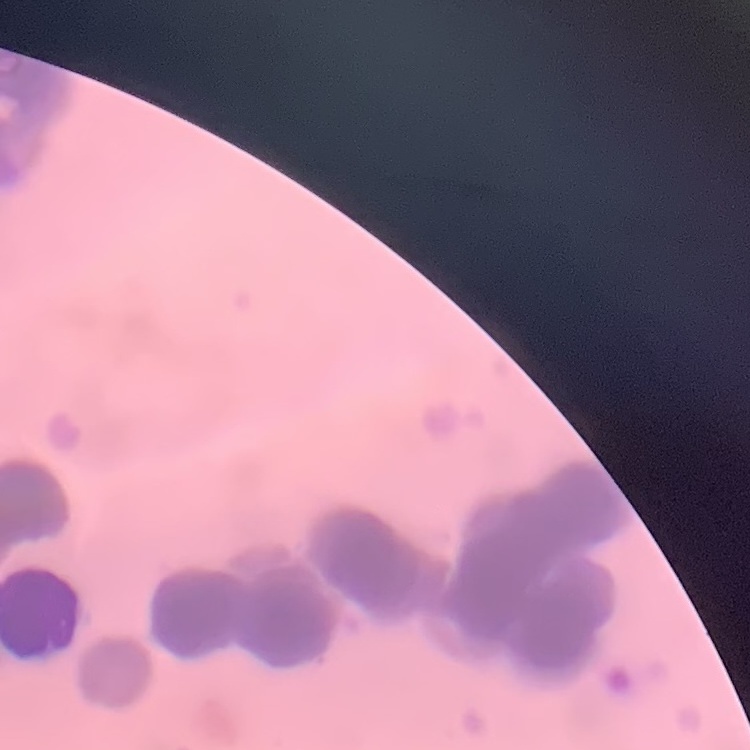

Summary:
  - Red blood cell morphology: rouleaux formation
  - Stain: Field's or Giemsa
  - Image type: one tile cut from a larger photomicrograph
  - Preparation: thin peripheral smear